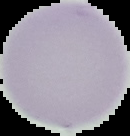

preparation = thin blood film
malaria status = uninfected
image size = 130×136 pixels
image type = segmented cell region with the area outside set to black